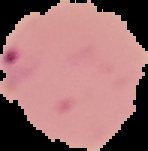
result = Plasmodium parasites detected
image type = segmented cell region with the area outside set to black
preparation = thin blood film
image size = 148×151 pixels